Point out each leukocyte.
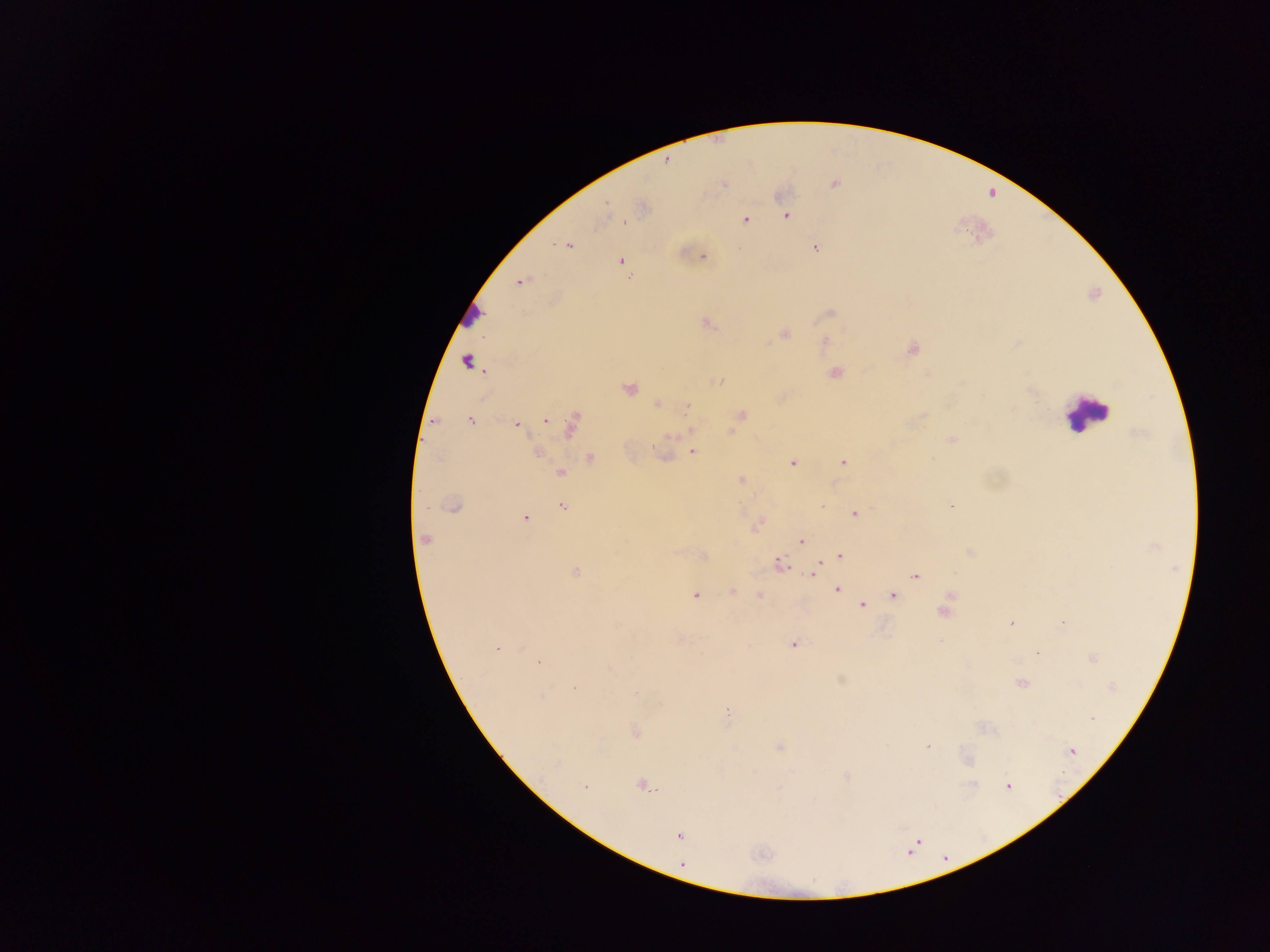
Approximate centers as x y in pixels.
Leukocytes: 470 311; 1084 413.

Plasmodium parasite locations: 666 161; 723 184; 835 184; 606 204; 787 216; 745 219; 568 246; 815 247; 702 256; 621 261; 630 277; 521 282; 829 313; 707 323; 784 334; 913 348; 467 362; 835 373; 720 382; 629 388; 1029 390; 658 403; 688 407; 742 414; 471 420; 545 420; 517 425; 571 425; 732 431; 952 439; 692 452; 536 453; 591 458; 843 462; 792 463; 560 473; 741 480; 454 507; 562 507; 821 507; 951 507; 855 514; 525 517; 425 539; 801 542; 839 556; 780 564; 815 570; 575 572; 915 575; 837 589; 733 591; 893 595; 695 596; 759 596; 862 605; 944 612; 1011 622; 1063 625; 793 644; 496 649; 1038 653; 1093 658; 539 662; 1020 684; 573 689; 636 693; 728 712; 1092 719; 635 732; 927 746; 780 747; 1072 752; 968 760; 846 776; 642 785; 585 786; 1008 786; 678 835; 682 865. Mobile-phone photograph taken through the microscope. Thick blood smear. One field of view. Sample from Ghana. Image is 1270×952 pixels.